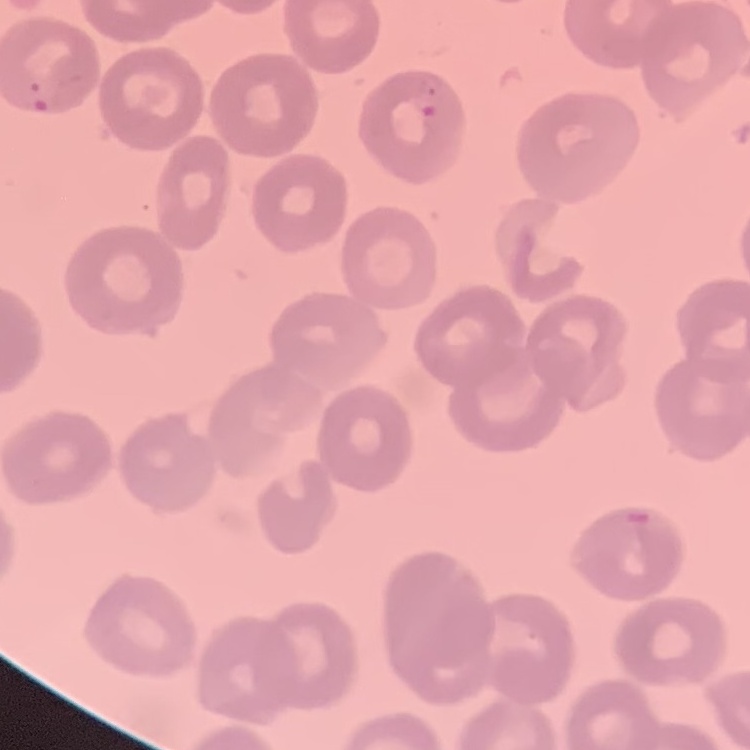

The red blood cells exhibit no rouleaux formation. One tile cut from a larger photomicrograph. Field's or Giemsa stain. Thin blood smear.